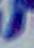
Micrograph. Toxoplasma gondii is seen. 1000x magnification.